Identify the preparation type.
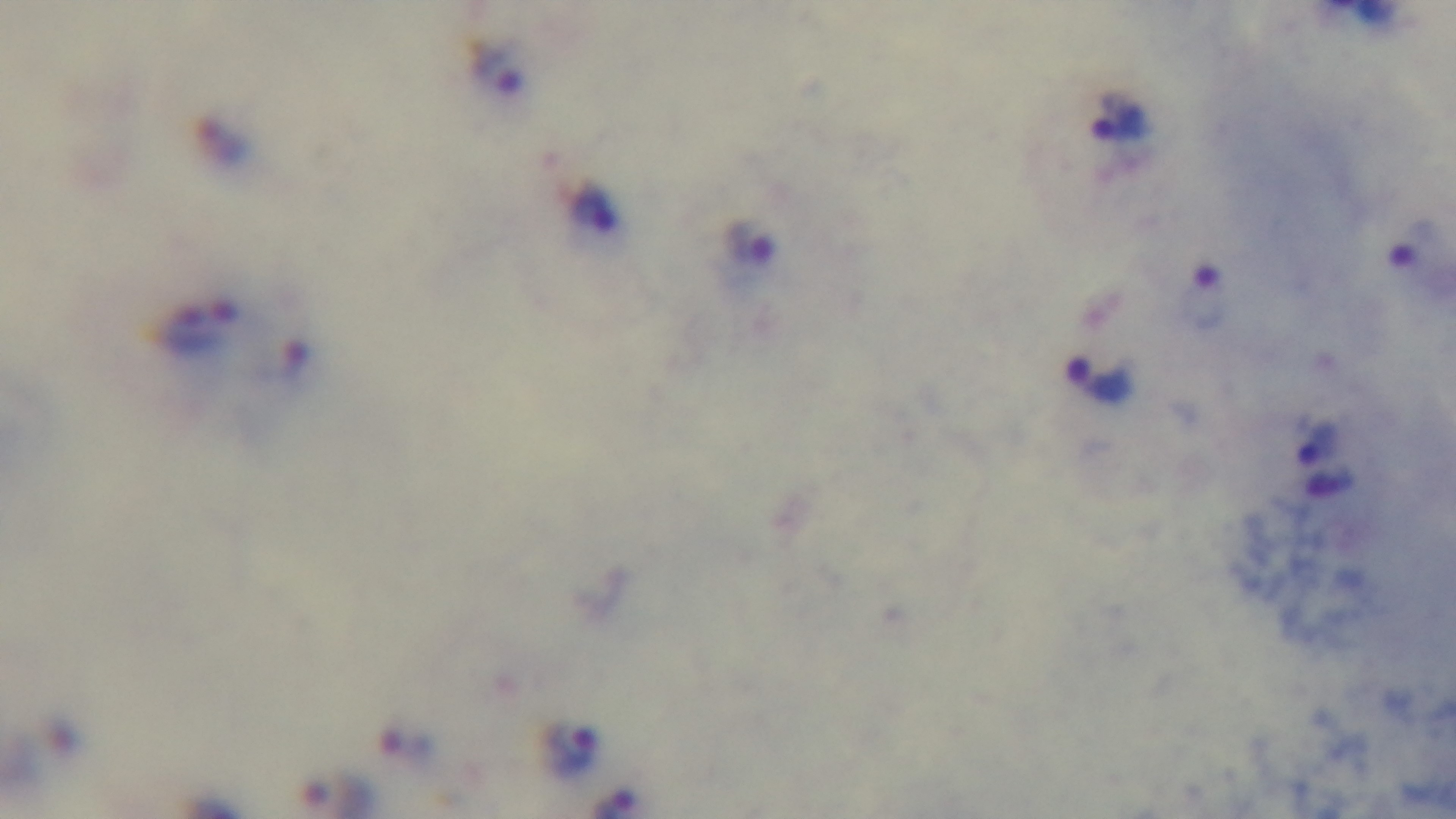

It is a thick blood film.

modality = light microscopy
objective = 100x oil immersion
field of view = one from the slide
capture = mounted 4K digital camera
stain = Giemsa
malaria status = positive